Assess this cell for malaria.
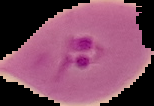

It is parasitized.

image size = 154×106 pixels
image type = segmented cell region on a black background
preparation = thin blood film